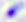
Micrograph. Toxoplasma gondii is seen. Captured at 400x magnification.